Comment on the morphology of the red blood cells.
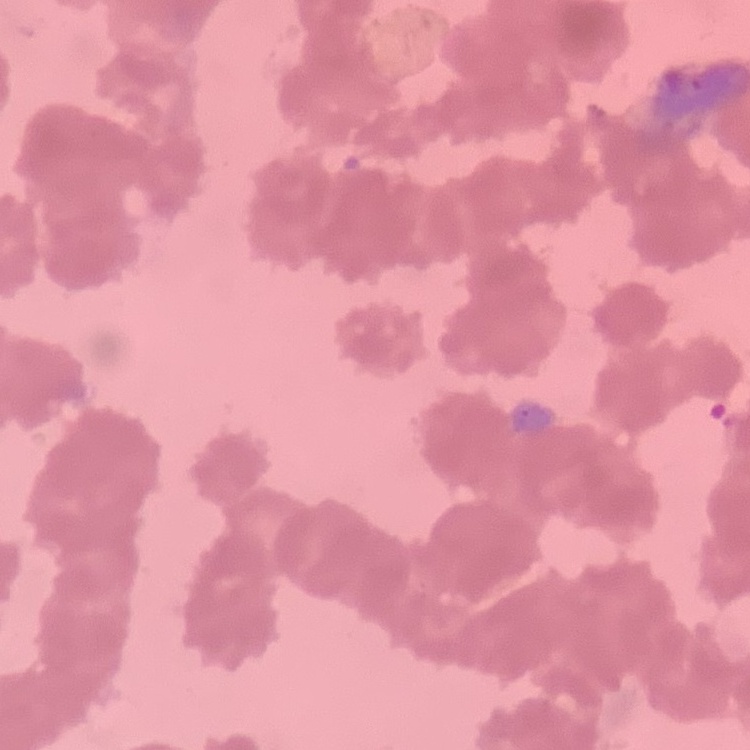

Rouleaux formation.

preparation = thin peripheral smear
image type = one tile cut from a larger photomicrograph
stain = Field's or Giemsa